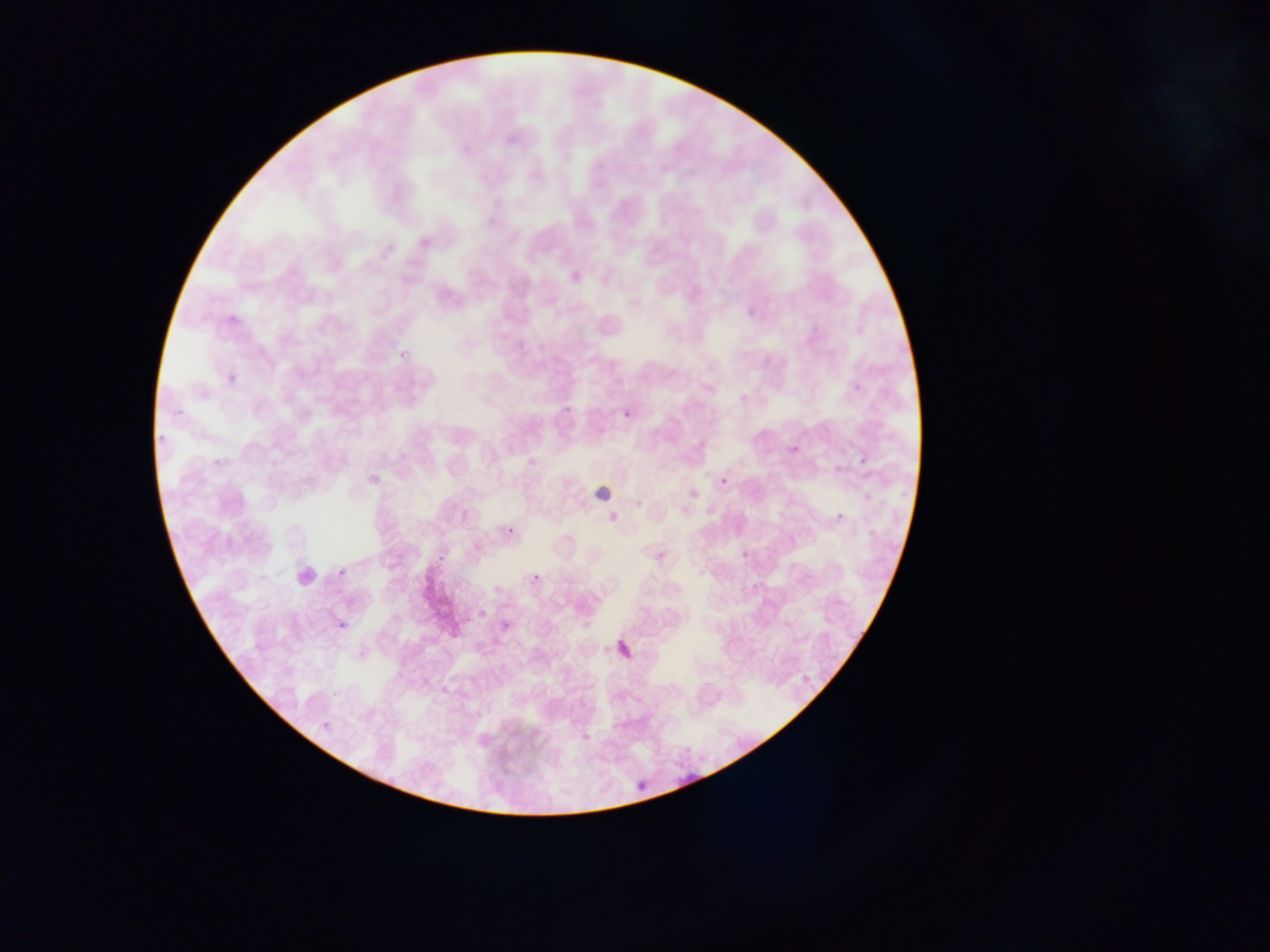 Approximate bounding boxes as {left, top, right, bottom} in pixels. Malaria parasite locations: {744, 304, 761, 322}, {227, 308, 251, 325}, {852, 378, 869, 391}, {619, 405, 638, 427}, {789, 444, 807, 457}, {856, 452, 874, 473}, {721, 459, 741, 486}, {831, 507, 851, 528}, {501, 522, 521, 542}, {652, 547, 671, 570}, {738, 551, 747, 559}, {332, 562, 351, 584}, {530, 571, 545, 586}, {478, 610, 495, 622}, {498, 614, 519, 640}, {334, 615, 354, 636}, {612, 638, 643, 669}, {798, 669, 820, 689}, {633, 777, 653, 799}. One field of view. Mobile-phone photograph taken through the microscope. Sample from Ghana. Image is 1270×952 pixels. Thin blood smear.